Give the position of every Plasmodium parasite.
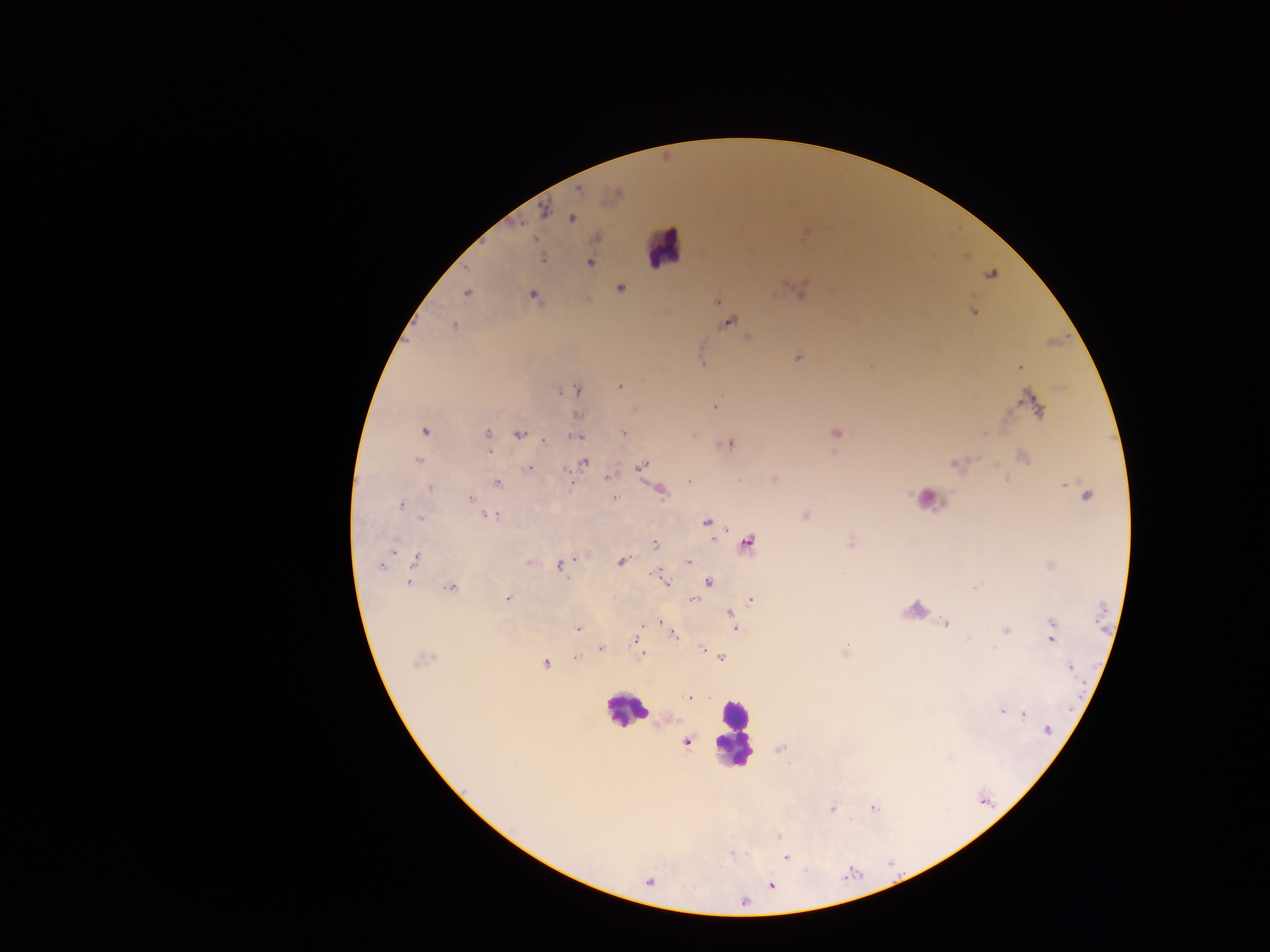
Approximate centers as [x, y] in pixels.
Plasmodium parasites: [544, 212], [572, 219], [541, 257], [589, 263], [621, 289], [465, 293], [800, 293], [533, 296], [717, 302], [972, 311], [728, 323], [454, 326], [748, 337], [797, 358], [1019, 367], [620, 386], [576, 390], [714, 406], [1036, 406], [577, 415], [424, 431], [488, 433], [624, 433], [837, 434], [520, 435], [575, 436], [544, 440], [729, 445], [489, 451], [1023, 457], [418, 460], [584, 462], [955, 464], [641, 467], [529, 468], [607, 478], [689, 482], [497, 483], [430, 488], [661, 491], [1086, 495], [615, 497], [470, 499], [400, 505], [492, 516], [805, 516], [421, 518], [707, 522], [654, 543], [748, 543], [416, 559], [529, 562], [621, 562], [689, 562], [381, 565], [561, 565], [664, 580], [709, 582], [408, 583], [975, 587], [450, 588], [507, 599], [751, 599], [693, 600], [730, 614], [661, 622], [946, 623], [734, 626], [1053, 627], [578, 628], [1005, 630], [639, 634], [674, 635], [1052, 637], [636, 640], [600, 649], [995, 649], [703, 650], [641, 653], [575, 657], [721, 658], [420, 661], [545, 663], [1070, 667], [690, 697], [1002, 711], [1024, 714], [1048, 731], [686, 741], [832, 808], [779, 836], [785, 857], [772, 885], [743, 902].

country = Ghana
field of view = single
image size = 1270×952 pixels
leukocyte locations = approximate centers as [x, y] in pixels: [664, 248], [625, 711], [733, 732]
capture = mobile-phone photograph through a microscope
preparation = thick blood smear